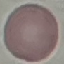

{
  "malaria_status": "uninfected",
  "preparation": "thin blood smear",
  "image_type": "automatically extracted cell patch, resized to 64 × 64 pixels",
  "capture": "smartphone camera at the microscope eyepiece",
  "stain": "Giemsa"
}